Assess the morphology of the erythrocytes.
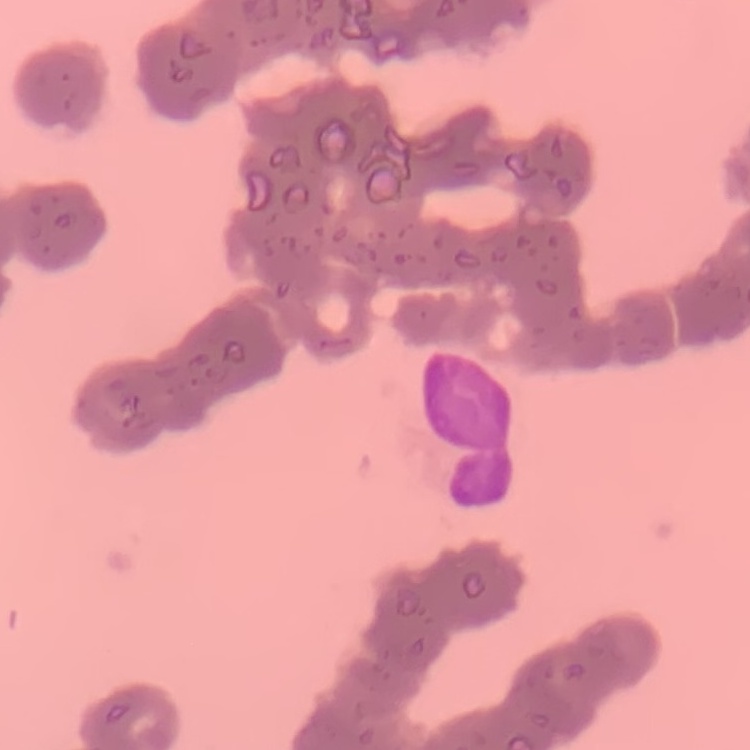

They show rouleaux formation.

Summary:
  - Stain: Field's or Giemsa
  - Image type: square crop of a larger photomicrograph
  - Preparation: thin blood film